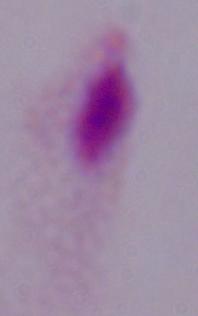
Summary:
  - Magnification: 1000x
  - Identification: trichomonad
  - Modality: micrograph